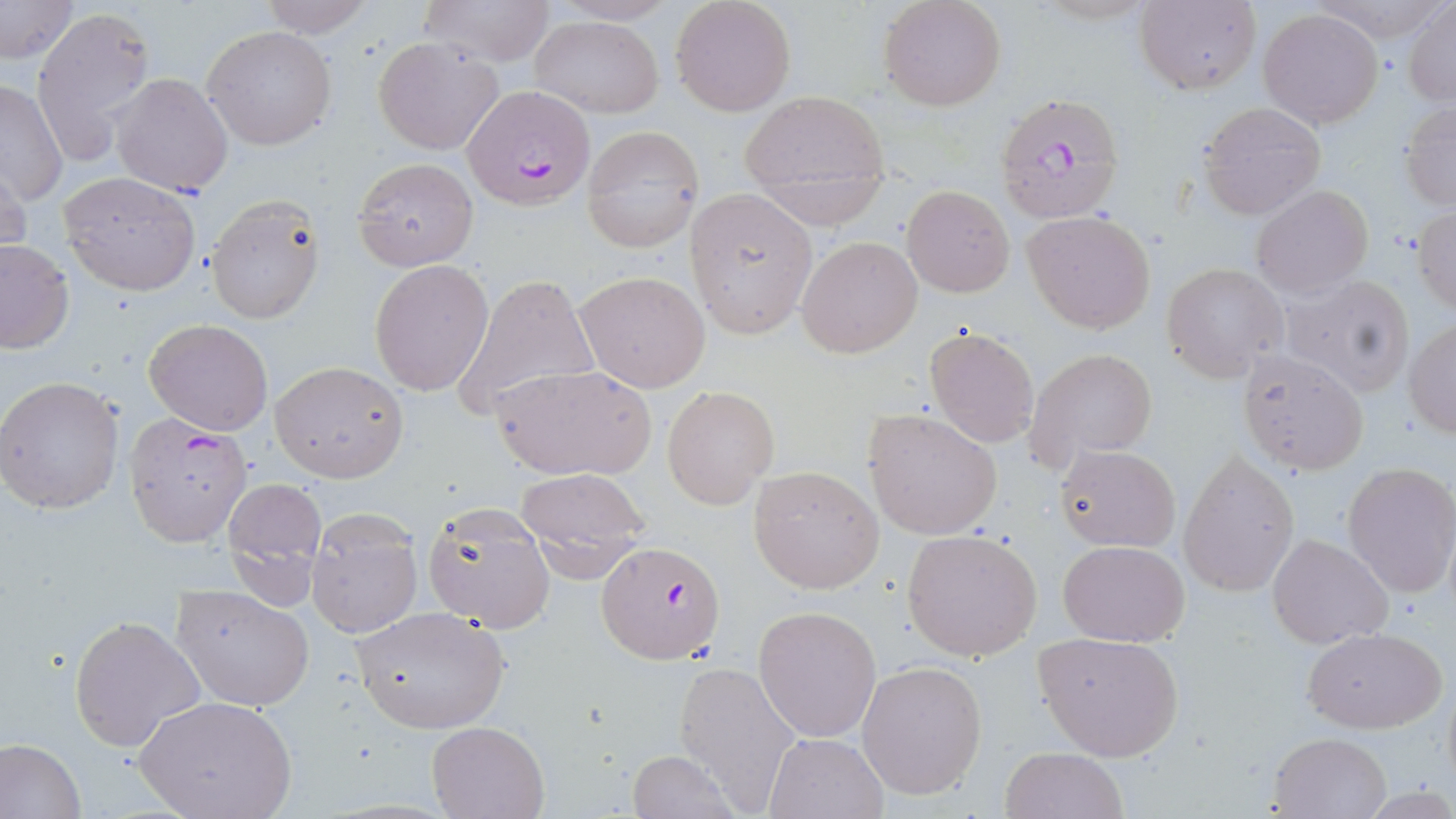
{
  "slide_level_diagnosis": "Plasmodium falciparum",
  "magnification": "1000x",
  "modality": "optical microscopy",
  "preparation": "thin blood smear",
  "image_size": "1456×819 pixels",
  "uninfected_red_blood_cell_locations": "approximate bounding boxes as (x1,y1)-(x2,y2) corner pairs in pixels: (253,0)-(376,38), (417,0)-(557,67), (670,0)-(796,117), (877,0)-(1007,112), (0,1)-(79,64), (1133,2)-(1261,94), (1405,2)-(1456,106), (32,5)-(155,166), (1257,8)-(1383,128), (530,16)-(663,117), (202,25)-(336,150), (373,37)-(504,155), (110,73)-(234,195), (1,79)-(69,207), (738,90)-(890,218), (1197,102)-(1326,220), (1400,103)-(1456,209), (581,126)-(704,252), (0,155)-(29,269), (353,157)-(479,271), (59,171)-(200,296), (900,183)-(1014,298), (1251,184)-(1374,298), (683,187)-(818,340), (207,196)-(325,325), (1411,207)-(1456,312), (1023,209)-(1157,334), (796,236)-(922,358), (0,239)-(74,354), (369,259)-(495,397), (1162,263)-(1287,381), (574,271)-(713,393), (1281,273)-(1415,396), (453,275)-(597,423), (143,318)-(275,436), (1405,319)-(1456,438), (922,324)-(1040,449), (1023,347)-(1160,474), (1233,348)-(1371,477), (269,362)-(408,482), (490,363)-(657,482), (0,375)-(124,516), (662,385)-(777,509), (862,407)-(1005,539), (1054,444)-(1180,551), (1178,451)-(1299,597), (1341,462)-(1456,598), (749,463)-(885,594), (513,467)-(652,577), (222,475)-(328,587), (422,502)-(555,631), (306,511)-(422,638), (902,529)-(1043,661), (1266,533)-(1394,648), (1057,539)-(1190,646), (172,586)-(313,711), (349,605)-(511,734), (754,605)-(882,742), (68,615)-(206,752), (1301,626)-(1446,733), (1033,630)-(1185,760), (855,660)-(986,801), (672,661)-(804,809), (133,696)-(297,819), (427,721)-(548,819), (763,731)-(887,818), (1267,731)-(1392,817), (0,738)-(85,818), (999,747)-(1129,819), (625,750)-(741,819)",
  "plasmodium_falciparum_infected_red_blood_cell_locations": "approximate bounding boxes as (x1,y1)-(x2,y2) corner pairs in pixels: (462,85)-(595,211), (998,94)-(1126,226), (126,412)-(256,545), (596,542)-(724,666)",
  "field_of_view": "one of a larger specimen",
  "stain": "May-Grünwald-Giemsa"
}